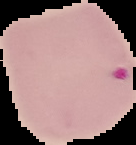
From a thin blood film. Malaria status: parasitized. Image is 136×145 pixels. The area outside the segmented cell region is set to black.